Report the malaria status of this cell.
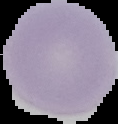
Uninfected.

preparation = thin blood film
image type = cell region segmented out of the field of view; surrounding area masked to black
image size = 118×124 pixels